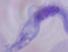

magnification = 1000x
identification = trypanosome
modality = micrograph